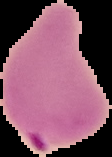 Result: malaria parasites identified. The area outside the segmented cell region is set to black. Image is 112×157 pixels. From a thin blood film.